State the preparation type.
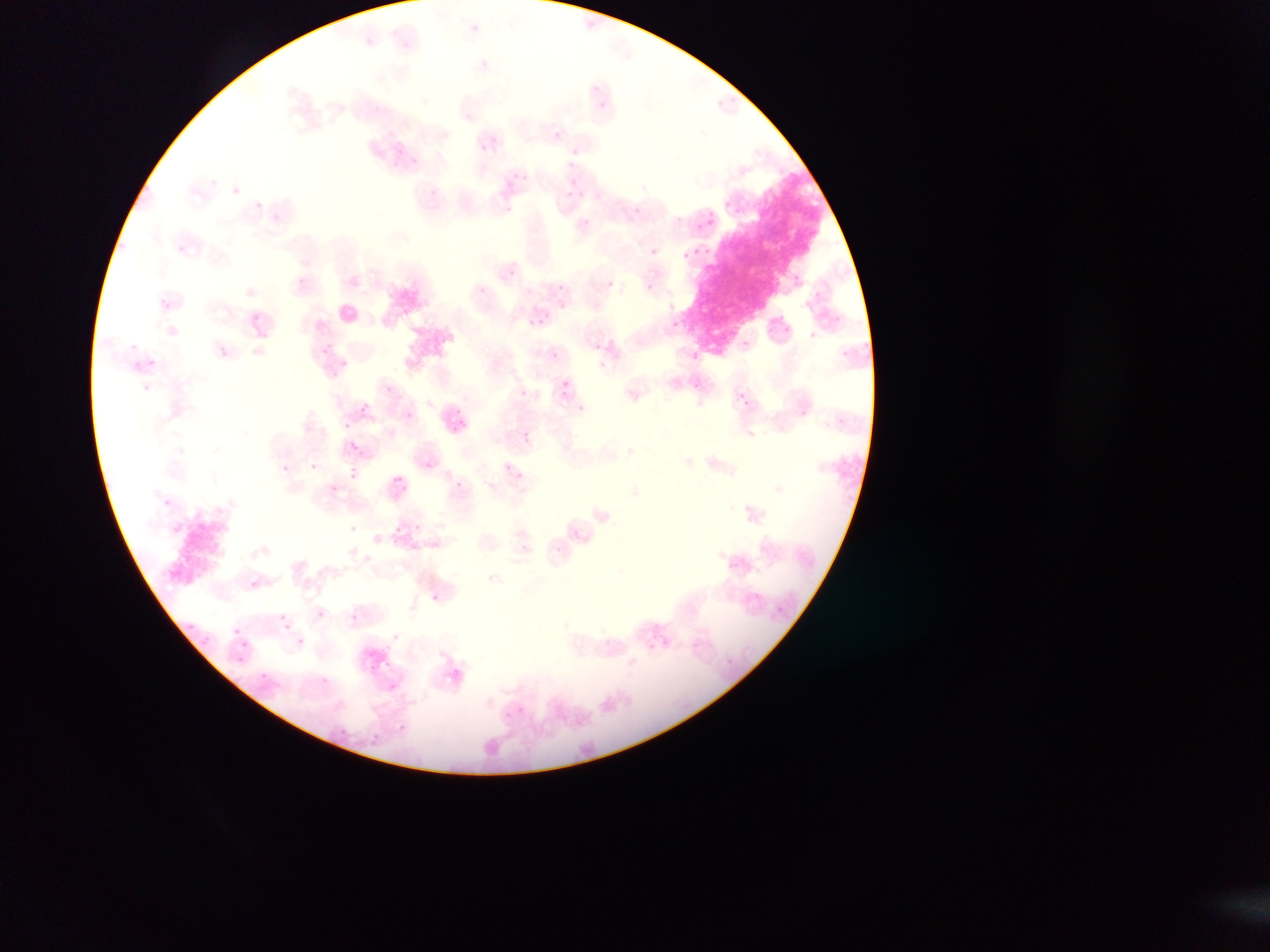

Thin blood film.

Approximate bounding boxes as left top right bottom in pixels.
Summary:
  - Malaria parasite locations: 480 61 487 69; 465 113 473 121; 554 130 562 139; 491 135 499 142; 479 144 486 152; 570 147 578 155; 410 159 418 166; 520 173 527 181; 565 189 573 197; 634 207 642 214; 271 214 279 220; 650 248 658 255; 297 276 305 284; 794 276 802 284; 606 280 614 288; 646 284 654 292; 247 289 256 296; 161 299 169 307; 558 300 566 307; 252 313 260 320; 673 320 682 328; 741 339 750 348; 595 342 602 350; 321 346 329 355; 219 348 227 356; 549 349 557 357; 149 357 157 365; 333 369 341 377; 562 380 570 388; 692 380 700 389; 142 383 150 392; 384 384 393 393; 520 388 528 395; 739 393 747 403; 740 396 749 405; 360 404 368 413; 405 411 413 419; 524 431 532 440; 350 442 358 451; 310 462 319 469; 282 464 290 472; 349 471 357 479; 394 476 402 483; 330 483 338 491; 414 523 422 530; 349 524 358 532; 729 560 737 568; 249 580 257 587; 431 594 439 600; 316 610 324 618; 350 615 358 622; 392 633 400 642; 296 637 304 646; 320 677 328 683; 516 707 525 716; 398 725 406 733; 339 729 347 737 | approximate x y pixel centers of objects too small to bound: 475 27; 596 89; 376 108; 212 182; 236 190; 259 207; 180 248; 788 329; 812 334; 843 353; 344 361; 601 365; 581 407; 802 413; 346 424; 525 549; 557 549; 283 617; 655 626; 237 631; 263 676
  - Artifact (stain precipitate or debris) locations: 699 180 813 345
  - Image size: 1270×952 pixels
  - Field of view: single
  - Capture: mobile-phone photograph through a microscope
  - Country: Ghana